Identify the blood parasite species.
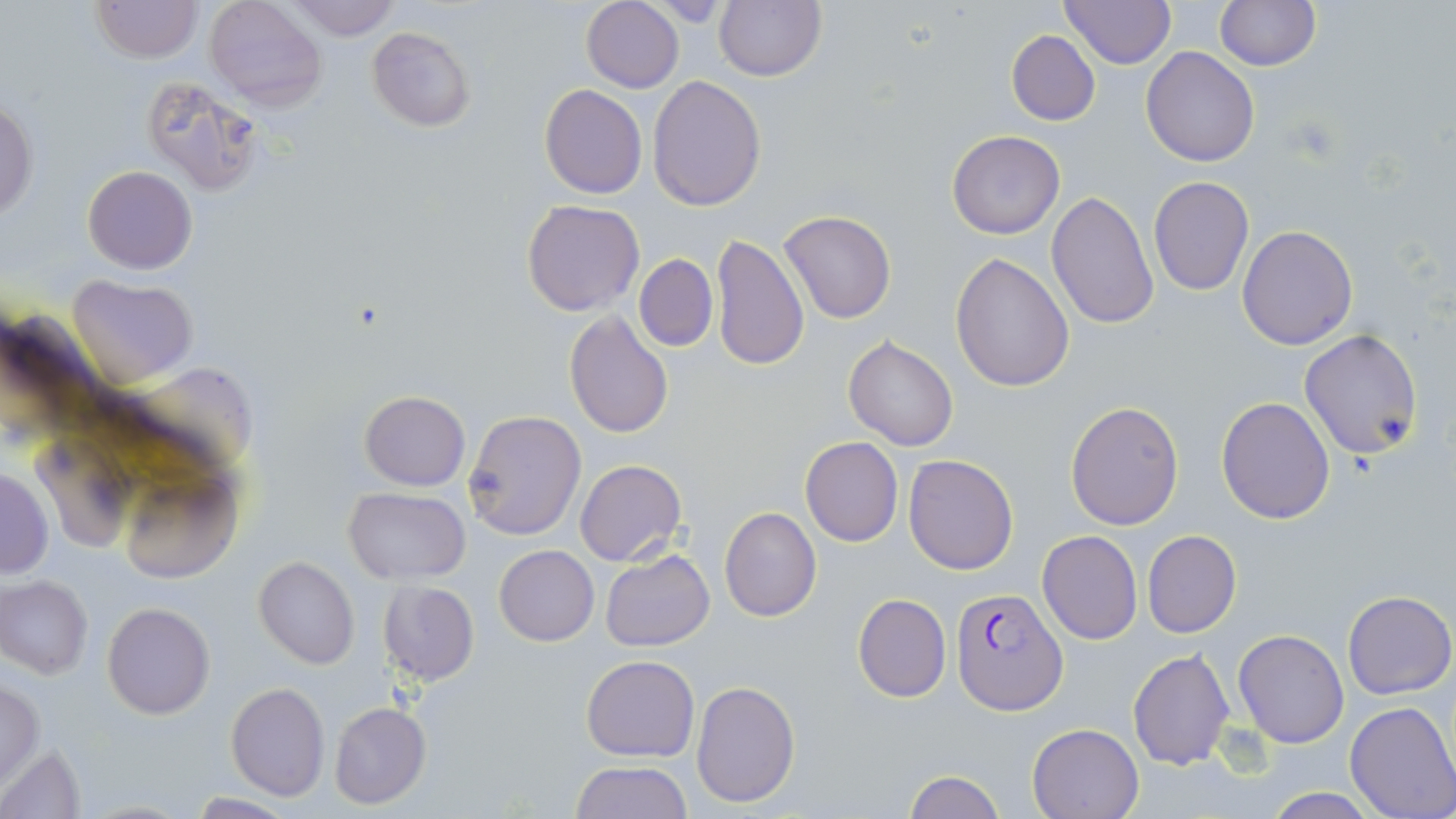

Plasmodium falciparum.

Approximate bounding boxes as [x1, y1, x2, y2] in pixels. Uninfected red blood cell locations: [90, 0, 201, 62], [203, 0, 327, 112], [285, 0, 401, 42], [1060, 0, 1176, 69], [581, 1, 684, 92], [714, 1, 825, 81], [1214, 1, 1321, 70], [366, 27, 476, 131], [1006, 30, 1100, 127], [1140, 46, 1260, 166], [141, 72, 263, 195], [647, 75, 766, 212], [539, 85, 648, 198], [0, 102, 38, 224], [946, 130, 1066, 240], [83, 166, 196, 273], [1147, 176, 1254, 296], [1046, 190, 1159, 329], [521, 200, 645, 317], [780, 209, 896, 323], [1237, 226, 1358, 349], [711, 233, 810, 372], [633, 254, 718, 350], [950, 254, 1075, 394], [68, 276, 197, 385], [564, 308, 673, 439], [1299, 330, 1424, 459], [843, 335, 960, 452], [118, 365, 253, 462], [359, 391, 470, 491], [1216, 395, 1335, 523], [1064, 400, 1183, 530], [462, 409, 587, 542], [800, 438, 903, 547], [33, 442, 138, 552], [903, 455, 1017, 574], [575, 459, 686, 565], [116, 463, 246, 583], [0, 469, 52, 579], [343, 488, 472, 583], [718, 505, 821, 622], [1036, 530, 1144, 645], [1142, 530, 1241, 639], [494, 545, 599, 646], [600, 549, 715, 652], [254, 556, 360, 669], [1, 576, 93, 678], [377, 580, 480, 685], [1343, 590, 1455, 700], [853, 593, 951, 703], [101, 602, 214, 718], [1233, 629, 1348, 748], [1128, 648, 1234, 771], [581, 654, 698, 762], [691, 679, 802, 807], [0, 680, 44, 788], [226, 683, 329, 800], [1345, 701, 1456, 819], [329, 702, 432, 810], [1027, 721, 1145, 818], [1, 741, 86, 819], [571, 760, 692, 818], [903, 771, 1007, 819], [1256, 789, 1388, 818], [187, 794, 299, 817]. Plasmodium falciparum-infected red blood cell locations: [952, 587, 1067, 714]. Thin blood smear. Image is 1456×819 pixels. May-Grünwald-Giemsa stain. 1000x magnification. Single field of view. Optical microscopy.